State the blood parasite species.
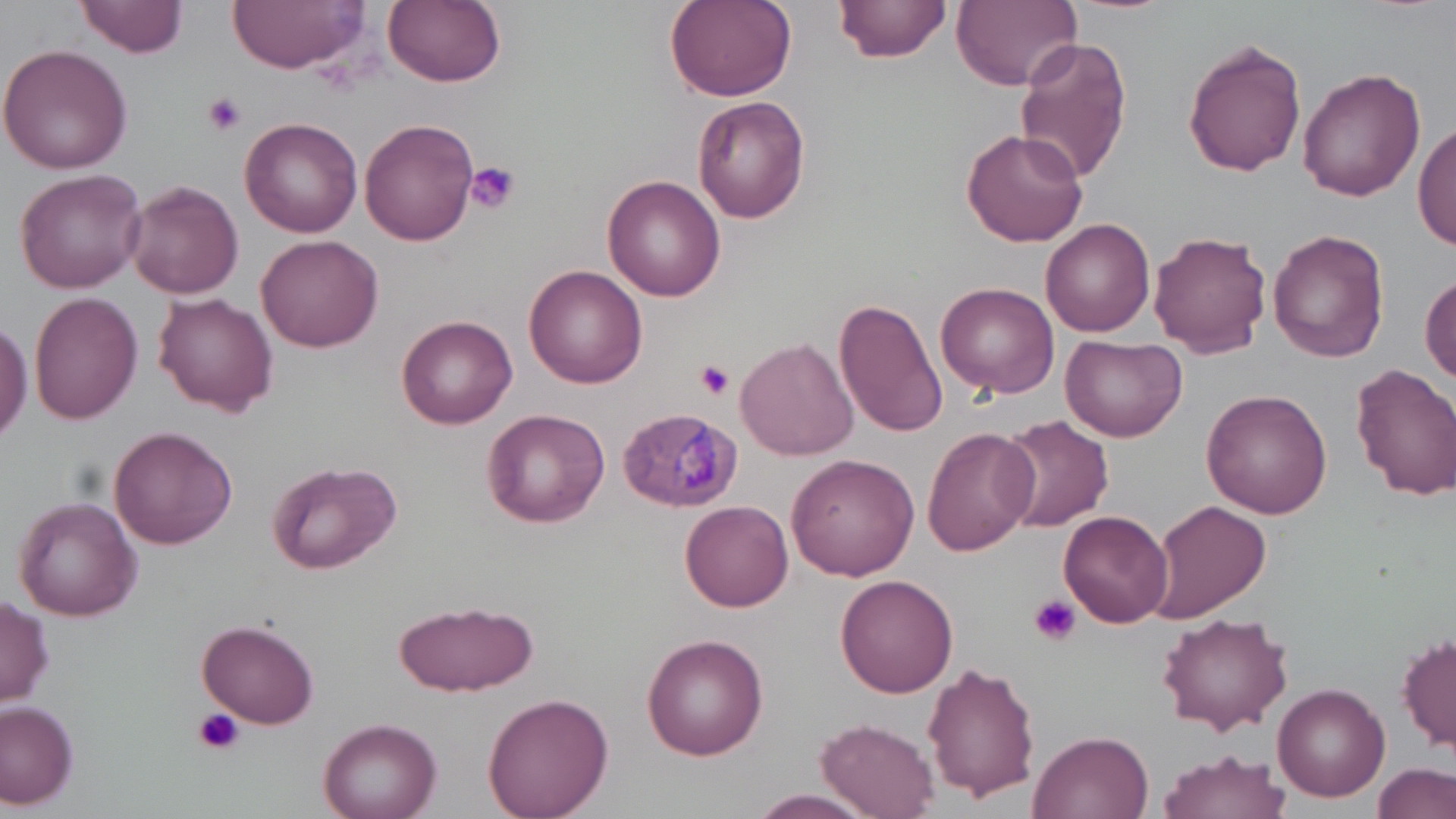
Plasmodium malariae.

field of view = one of a larger specimen
modality = light microscopy
Plasmodium malariae-infected red blood cell locations = approximate bounding boxes as (x1, y1, x2, y2) in pixels: (618, 405, 740, 511)
stain = May-Grünwald-Giemsa
magnification = 1000x
platelet locations = approximate bounding boxes as (x1, y1, x2, y2) in pixels: (202, 93, 248, 136), (463, 161, 520, 213), (693, 360, 734, 399), (1030, 594, 1081, 647), (193, 707, 244, 757)
preparation = thin blood film
uninfected red blood cell locations = approximate bounding boxes as (x1, y1, x2, y2) in pixels: (76, 0, 187, 58), (227, 0, 369, 71), (383, 0, 506, 88), (664, 0, 798, 102), (837, 0, 950, 65), (950, 0, 1082, 90), (1013, 37, 1134, 186), (1183, 38, 1307, 179), (0, 43, 132, 176), (1298, 66, 1426, 202), (693, 96, 811, 224), (238, 117, 364, 238), (361, 118, 481, 247), (1414, 119, 1456, 253), (962, 125, 1089, 247), (13, 169, 149, 294), (603, 174, 725, 301), (124, 179, 244, 299), (1041, 217, 1155, 337), (1266, 229, 1390, 364), (1149, 231, 1272, 357), (255, 234, 383, 351), (525, 265, 648, 389), (1421, 269, 1456, 387), (937, 282, 1058, 399), (153, 291, 278, 416), (26, 292, 142, 427), (833, 296, 945, 439), (396, 315, 518, 430), (0, 316, 32, 448), (1059, 332, 1185, 440), (736, 336, 858, 461), (1352, 363, 1456, 501), (1203, 389, 1331, 517), (480, 409, 610, 529), (994, 414, 1110, 533), (108, 426, 240, 550), (922, 427, 1036, 556), (787, 454, 918, 581), (265, 461, 402, 575), (12, 495, 145, 621), (680, 499, 794, 612), (1147, 501, 1271, 623), (1059, 508, 1174, 628), (836, 575, 958, 696), (0, 596, 54, 707), (392, 601, 537, 697), (1156, 612, 1296, 737), (198, 619, 319, 730), (1398, 632, 1456, 754), (640, 633, 768, 760), (923, 660, 1039, 801), (1272, 682, 1392, 802), (483, 691, 614, 818), (0, 701, 79, 809), (317, 718, 441, 819), (817, 718, 938, 817), (1029, 730, 1154, 819), (1157, 750, 1290, 819), (1373, 761, 1455, 819), (746, 789, 880, 817)
image size = 1456×819 pixels